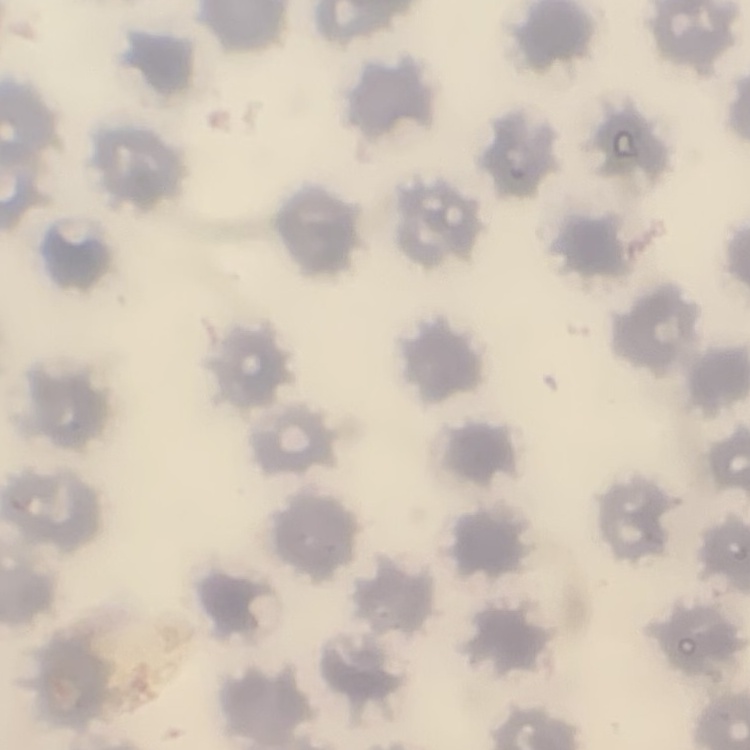

Summary:
  - Erythrocyte morphology: no rouleaux formation
  - Preparation: thin blood film
  - Stain: Field's or Giemsa
  - Image type: one tile cut from a larger photomicrograph